Classify the preparation.
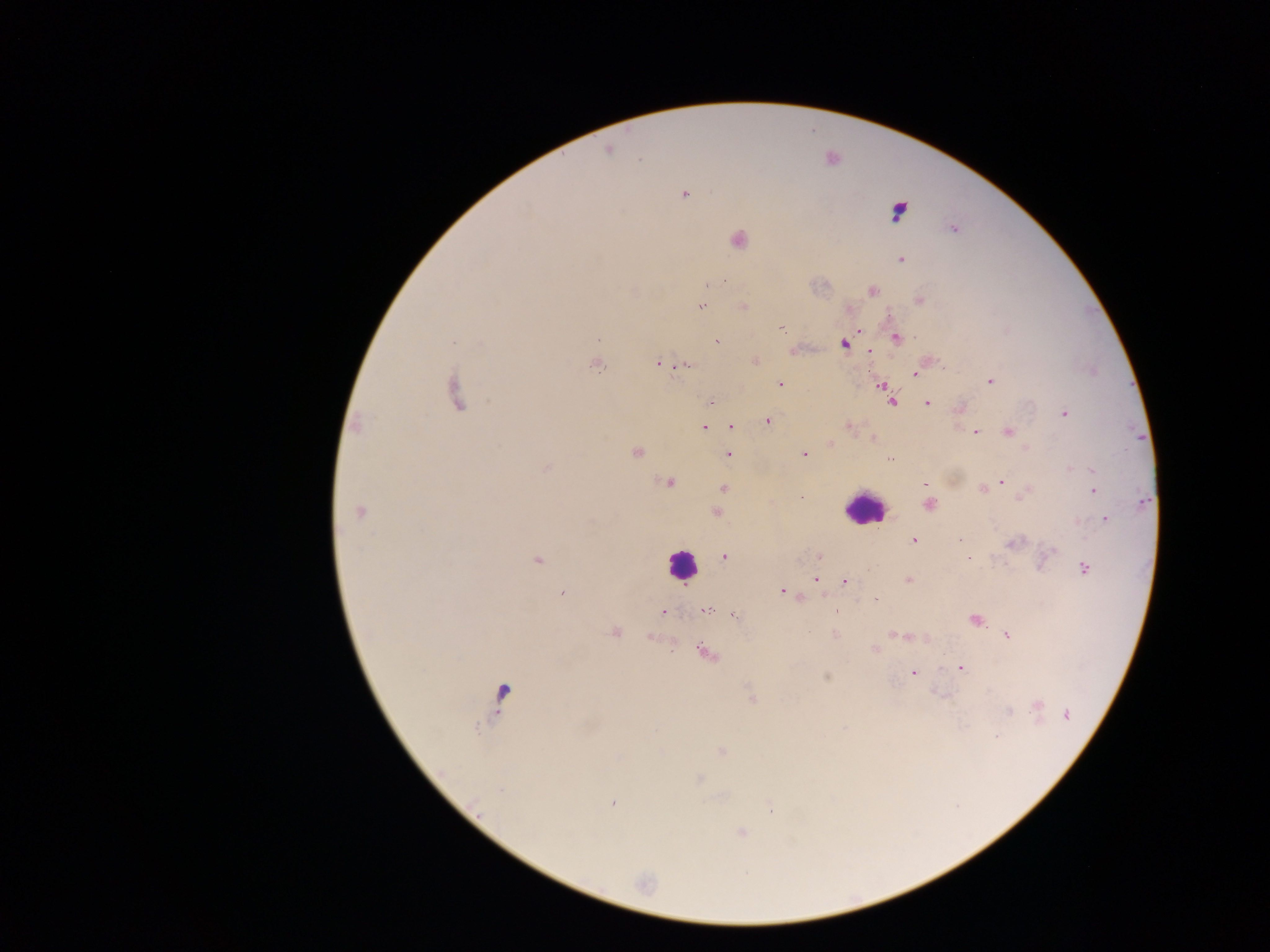

Thick blood film.

image size = 1270×952 pixels
leukocyte locations = approximate centers as x y in pixels: 862 508; 681 564
country = Ghana
malaria parasite locations = approximate centers as x y in pixels: 608 150; 639 159; 685 194; 898 211; 954 229; 738 240; 901 260; 724 281; 712 284; 872 291; 919 300; 744 306; 701 307; 781 327; 860 330; 897 338; 717 341; 844 343; 870 351; 756 362; 658 364; 597 365; 687 365; 914 373; 990 381; 780 383; 881 385; 457 393; 710 402; 892 402; 927 403; 1065 414; 768 421; 356 426; 732 427; 848 427; 703 428; 975 432; 1008 432; 873 438; 830 444; 636 452; 803 454; 728 455; 890 459; 1071 469; 1091 469; 668 482; 1002 482; 926 484; 724 489; 983 489; 1094 490; 801 497; 1143 501; 929 505; 360 512; 717 512; 1105 519; 914 540; 960 540; 1014 543; 1051 551; 725 557; 819 557; 968 558; 537 560; 1084 567; 815 579; 908 579; 845 581; 783 591; 561 594; 876 601; 705 610; 663 611; 736 617; 975 619; 615 632; 835 634; 895 634; 1008 636; 875 649; 706 653; 961 668; 913 673; 826 677; 502 695; 751 696; 1037 705; 1008 711; 1067 715; 997 737; 722 751; 699 779; 501 791; 613 802; 741 833
field of view = single
capture = mobile-phone photograph through a microscope